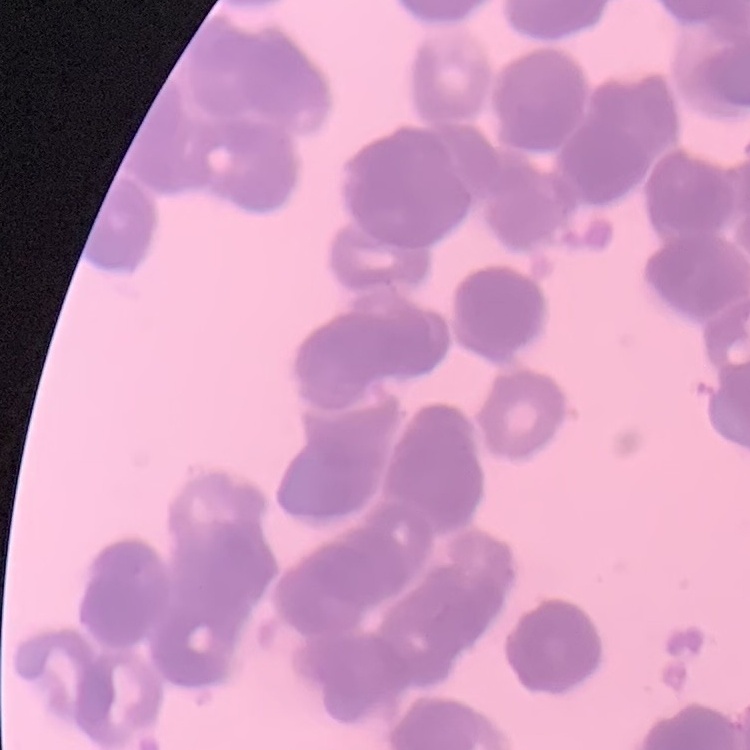

The red blood cells show rouleaux formation. Thin blood smear. Field's or Giemsa stain. One tile cut from a larger photomicrograph.